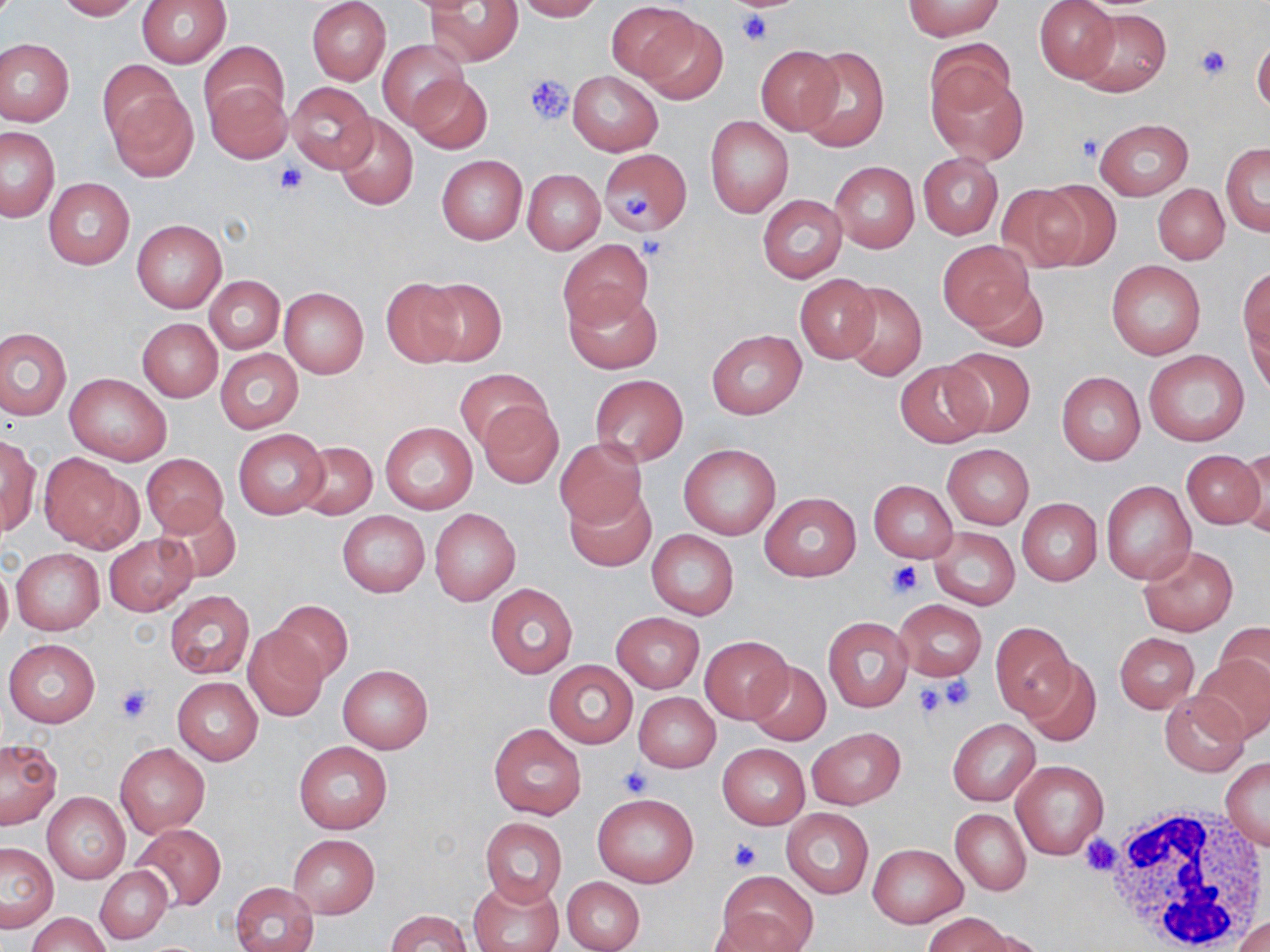
Summary:
  - Coordinate format: approximate bounding boxes as (x1, y1, x2, y2) in pixels
  - Uninfected red blood cell locations: (54, 0, 142, 20), (135, 0, 232, 67), (307, 0, 391, 85), (515, 0, 603, 21), (904, 0, 1004, 39), (428, 1, 523, 68), (1035, 1, 1118, 82), (606, 2, 700, 82), (1076, 8, 1170, 95), (633, 10, 728, 104), (1252, 37, 1270, 115), (0, 39, 74, 127), (378, 39, 468, 128), (924, 40, 1017, 128), (198, 41, 289, 125), (754, 45, 844, 134), (797, 45, 889, 152), (98, 59, 180, 144), (927, 68, 1027, 163), (568, 71, 663, 155), (407, 74, 491, 154), (206, 80, 292, 165), (285, 81, 377, 172), (106, 88, 199, 182), (333, 115, 418, 210), (705, 115, 794, 217), (1095, 118, 1194, 199), (0, 127, 60, 221), (1220, 142, 1270, 235), (599, 148, 690, 237), (436, 153, 527, 245), (917, 153, 1003, 239), (830, 161, 919, 253), (523, 170, 603, 254), (44, 178, 135, 269), (1031, 180, 1121, 269), (995, 184, 1090, 271), (1153, 184, 1228, 263), (758, 195, 847, 283), (131, 219, 226, 313), (561, 240, 653, 330), (939, 240, 1032, 332), (1106, 261, 1206, 360), (1240, 268, 1269, 358), (794, 274, 881, 363), (205, 276, 285, 353), (382, 277, 465, 367), (419, 277, 506, 367), (965, 280, 1050, 352), (840, 281, 927, 382), (564, 287, 662, 375), (279, 288, 368, 379), (1245, 303, 1269, 395), (137, 318, 222, 402), (0, 327, 71, 419), (706, 329, 807, 420), (941, 347, 1035, 436), (215, 348, 303, 433), (1143, 348, 1251, 447), (894, 361, 990, 447), (453, 368, 551, 450), (1057, 371, 1145, 465), (65, 372, 172, 465), (589, 373, 688, 467), (478, 400, 562, 488), (380, 422, 477, 515), (233, 430, 328, 518), (0, 436, 39, 537), (554, 437, 648, 530), (295, 439, 377, 518), (943, 443, 1034, 529), (679, 444, 780, 539), (1236, 448, 1269, 531), (1182, 451, 1265, 529), (38, 453, 140, 554), (141, 453, 229, 537), (868, 480, 957, 563), (1101, 480, 1196, 584), (564, 487, 656, 572), (758, 492, 862, 581), (1016, 498, 1102, 585), (155, 503, 241, 583), (430, 509, 520, 606), (337, 510, 430, 597), (928, 526, 1021, 608), (647, 529, 739, 619), (104, 534, 197, 615), (1138, 543, 1237, 636), (11, 549, 103, 634), (0, 560, 12, 647), (485, 582, 579, 678), (165, 591, 253, 677), (894, 598, 985, 681), (267, 599, 353, 682), (610, 613, 705, 694), (823, 617, 913, 711), (990, 621, 1078, 719), (1217, 622, 1270, 697), (242, 626, 329, 721), (1114, 632, 1199, 712), (700, 635, 792, 722), (3, 640, 99, 728), (1193, 654, 1270, 741), (1020, 657, 1102, 746), (544, 660, 637, 749), (747, 662, 831, 745), (338, 663, 433, 754), (173, 676, 262, 764), (634, 692, 720, 771), (1160, 692, 1250, 776), (948, 718, 1039, 805), (488, 723, 587, 820), (807, 726, 904, 809), (0, 739, 62, 828), (294, 741, 393, 834), (115, 743, 209, 837), (718, 744, 810, 829), (1220, 755, 1270, 849), (1010, 759, 1108, 859), (42, 793, 130, 884), (591, 793, 699, 887), (782, 808, 873, 898), (949, 808, 1031, 896), (480, 817, 566, 907), (133, 824, 225, 910), (287, 834, 379, 919), (0, 841, 58, 931), (867, 843, 966, 928), (95, 866, 171, 944), (715, 868, 818, 952), (561, 876, 646, 952), (470, 877, 565, 952), (230, 882, 319, 952), (386, 910, 472, 952), (708, 910, 806, 952), (29, 912, 110, 952), (924, 912, 1012, 952), (1234, 916, 1269, 952), (968, 930, 1048, 952)
  - Platelet locations: (731, 0, 794, 15), (738, 10, 771, 45), (1195, 44, 1229, 79), (524, 75, 574, 124), (1077, 133, 1104, 161), (277, 163, 306, 194), (622, 191, 651, 219), (885, 560, 921, 598), (938, 676, 975, 710), (115, 683, 155, 725), (915, 683, 949, 717), (617, 766, 653, 796), (1080, 834, 1121, 875), (728, 836, 762, 872)
  - White blood cell locations: (1095, 803, 1266, 950)
  - Slide-level diagnosis: no evidence of blood parasites
  - Magnification: 1000x
  - Field of view: single
  - Image size: 1270×952 pixels
  - Preparation: thin blood smear
  - Stain: May-Grünwald-Giemsa
  - Modality: optical microscopy